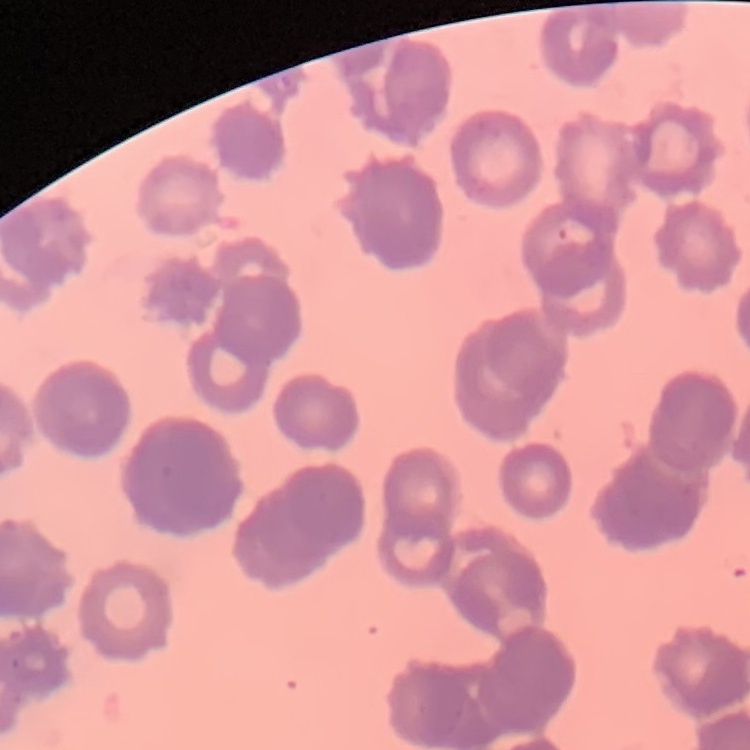
erythrocyte morphology = rouleaux formation
stain = Field's or Giemsa
preparation = thin blood smear
image type = square crop of a larger photomicrograph